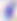
magnification: 400x
modality: micrograph
identification: Toxoplasma gondii